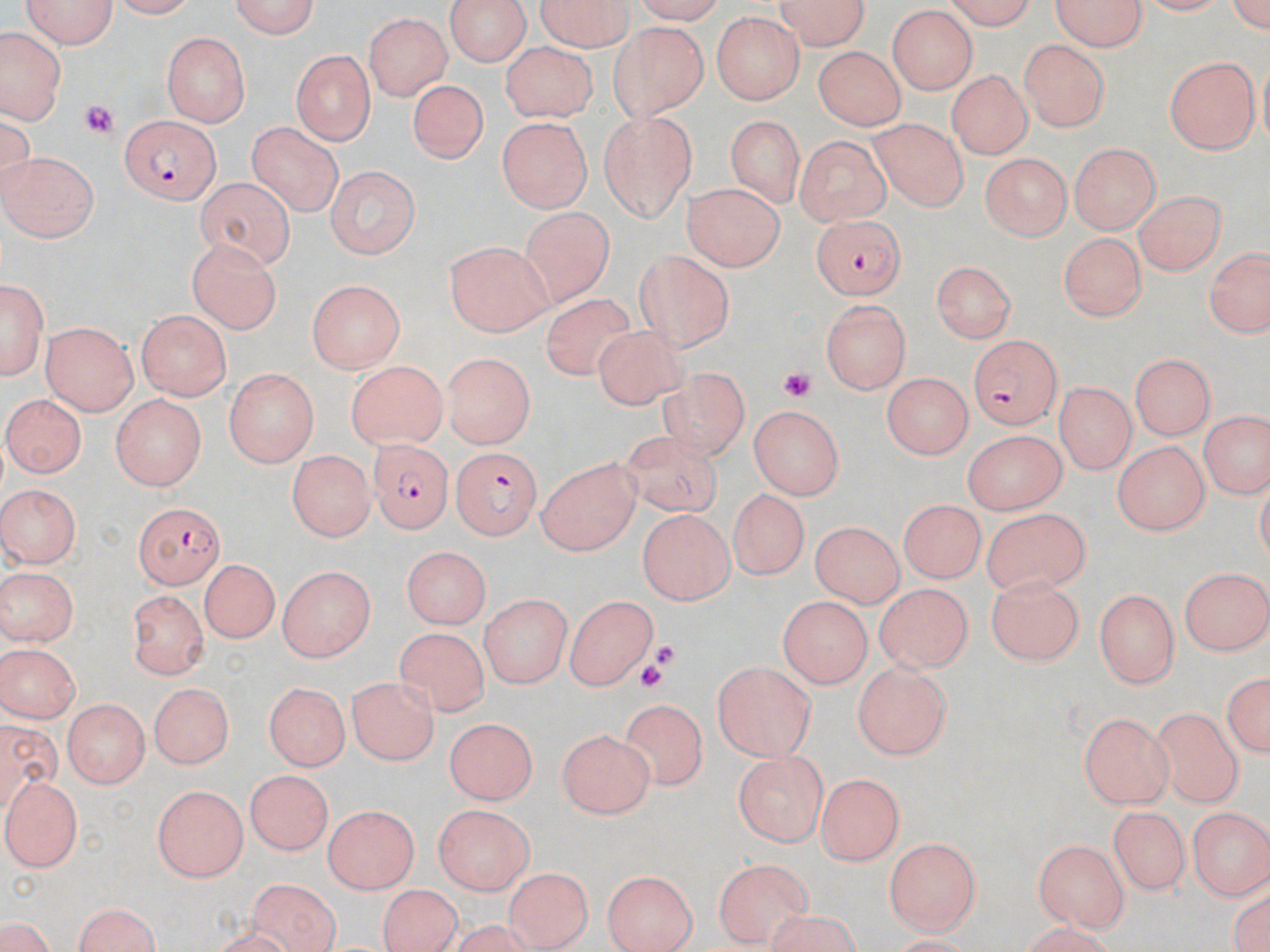
Approximate bounding boxes as [x1, y1, x2, y2] in pixels. Plasmodium falciparum-infected red blood cell locations: [121, 115, 220, 204], [806, 214, 908, 298], [969, 335, 1063, 428], [366, 439, 451, 537], [452, 447, 541, 539], [134, 501, 226, 589]. Platelet locations: [80, 102, 120, 143], [779, 368, 814, 401], [653, 641, 676, 668], [638, 663, 667, 695]. Uninfected red blood cell locations: [17, 0, 120, 50], [105, 0, 198, 18], [227, 0, 323, 39], [444, 0, 533, 66], [533, 0, 637, 51], [771, 0, 872, 49], [938, 0, 1042, 28], [1054, 0, 1149, 48], [886, 8, 976, 94], [362, 11, 451, 101], [710, 12, 805, 106], [606, 21, 707, 119], [3, 30, 61, 120], [162, 33, 252, 126], [1019, 38, 1114, 132], [499, 42, 601, 120], [812, 46, 906, 132], [293, 48, 375, 143], [1164, 55, 1258, 154], [945, 68, 1032, 159], [408, 79, 489, 169], [598, 109, 700, 219], [725, 115, 814, 211], [870, 119, 969, 212], [499, 120, 593, 215], [247, 123, 343, 218], [792, 132, 893, 222], [1068, 142, 1162, 235], [2, 151, 99, 244], [979, 153, 1069, 240], [322, 164, 421, 257], [192, 175, 296, 265], [686, 183, 784, 270], [1134, 191, 1223, 275], [514, 211, 614, 305], [1059, 229, 1149, 317], [189, 240, 283, 335], [444, 241, 553, 336], [1204, 241, 1269, 337], [633, 254, 737, 351], [928, 261, 1018, 343], [1, 274, 47, 379], [307, 279, 403, 373], [539, 294, 642, 380], [819, 298, 914, 395], [136, 311, 228, 399], [40, 321, 140, 413], [591, 328, 692, 409], [1130, 351, 1215, 439], [440, 352, 533, 448], [347, 363, 448, 451], [225, 368, 320, 469], [656, 370, 755, 461], [883, 373, 970, 462], [1056, 383, 1135, 476], [6, 393, 86, 477], [109, 393, 207, 492], [748, 405, 843, 500], [1200, 410, 1266, 499], [963, 428, 1069, 514], [620, 431, 721, 516], [1113, 440, 1206, 536], [285, 449, 375, 543], [537, 453, 644, 554], [0, 484, 78, 568], [729, 486, 809, 576], [896, 501, 985, 582], [982, 505, 1088, 592], [635, 510, 737, 603], [812, 519, 907, 606], [398, 547, 489, 631], [202, 555, 277, 640], [277, 564, 373, 662], [1181, 564, 1269, 657], [1, 565, 77, 648], [985, 577, 1086, 666], [873, 582, 972, 674], [1095, 587, 1180, 686], [127, 588, 209, 679], [482, 593, 571, 690], [562, 594, 659, 691], [777, 594, 872, 687], [397, 626, 488, 712], [0, 643, 82, 721], [710, 661, 819, 765], [854, 662, 951, 761], [1221, 669, 1270, 763], [349, 674, 439, 763], [264, 680, 351, 767], [147, 681, 237, 770], [621, 696, 708, 789], [62, 703, 148, 789], [1151, 708, 1244, 809], [1077, 711, 1175, 810], [0, 717, 68, 809], [443, 718, 537, 806], [558, 726, 658, 819], [736, 749, 827, 847], [244, 771, 332, 857], [814, 772, 905, 866], [2, 776, 86, 871], [152, 783, 245, 882], [320, 802, 420, 892], [431, 802, 534, 897], [1106, 802, 1190, 891], [1189, 805, 1269, 901], [1033, 835, 1131, 931], [884, 837, 979, 936], [716, 862, 813, 946], [601, 869, 699, 952], [499, 875, 592, 952], [246, 877, 340, 952], [379, 885, 461, 952], [70, 902, 164, 952], [0, 917, 57, 952]. Slide-level diagnosis: Plasmodium falciparum. Single field of view. Optical microscopy. Captured at 1000x magnification. Thin blood smear. Image is 1270×952 pixels. May-Grünwald-Giemsa stain.